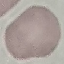

result: no malaria parasites detected
preparation: thin smear
stain: Giemsa
capture: smartphone camera at the microscope eyepiece
image_type: automatically extracted cell patch, resized to 64 × 64 pixels